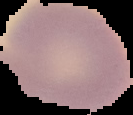

malaria status = uninfected
preparation = thin blood smear
image type = cell region segmented out of the field of view; surrounding area masked to black
image size = 133×115 pixels